Locate every blood parasite and identify its species.
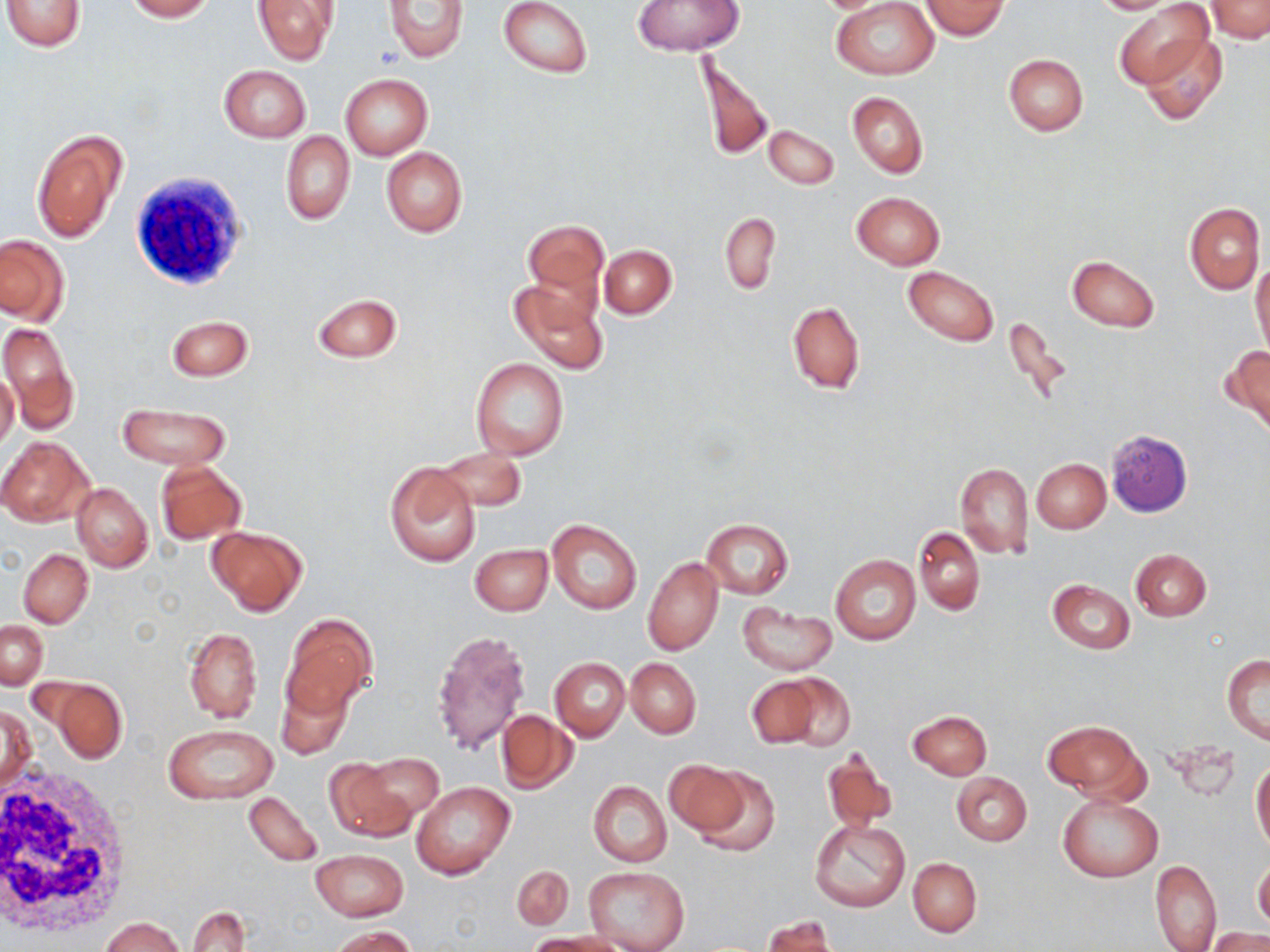

No blood parasites observed.

slide-level diagnosis = no evidence of blood parasites
stain = May-Grünwald-Giemsa
preparation = thin blood smear
white blood cell locations = approximate bounding boxes as named x1/y1/x2/y2 corners in pixels: (x1=129, y1=170, x2=247, y2=290), (x1=0, y1=766, x2=137, y2=936)
image size = 1270×952 pixels
field of view = single
magnification = 1000x
modality = optical microscopy
uninfected red blood cell locations = approximate bounding boxes as named x1/y1/x2/y2 corners in pixels: (x1=2, y1=0, x2=87, y2=52), (x1=123, y1=0, x2=213, y2=21), (x1=498, y1=0, x2=592, y2=78), (x1=1090, y1=0, x2=1180, y2=14), (x1=1205, y1=0, x2=1270, y2=42), (x1=251, y1=1, x2=337, y2=65), (x1=385, y1=1, x2=469, y2=61), (x1=633, y1=1, x2=744, y2=54), (x1=830, y1=1, x2=939, y2=80), (x1=921, y1=1, x2=1008, y2=39), (x1=1112, y1=1, x2=1213, y2=90), (x1=1138, y1=30, x2=1229, y2=125), (x1=695, y1=48, x2=774, y2=166), (x1=1003, y1=54, x2=1088, y2=136), (x1=218, y1=64, x2=311, y2=141), (x1=339, y1=73, x2=432, y2=160), (x1=846, y1=91, x2=927, y2=179), (x1=763, y1=125, x2=839, y2=189), (x1=31, y1=128, x2=127, y2=242), (x1=280, y1=132, x2=354, y2=225), (x1=381, y1=147, x2=468, y2=236), (x1=852, y1=192, x2=944, y2=268), (x1=1184, y1=202, x2=1265, y2=295), (x1=720, y1=213, x2=780, y2=294), (x1=521, y1=218, x2=609, y2=303), (x1=0, y1=235, x2=68, y2=324), (x1=599, y1=245, x2=676, y2=317), (x1=1067, y1=256, x2=1160, y2=331), (x1=1251, y1=261, x2=1270, y2=356), (x1=902, y1=267, x2=998, y2=346), (x1=509, y1=279, x2=607, y2=376), (x1=312, y1=294, x2=402, y2=363), (x1=786, y1=302, x2=865, y2=395), (x1=167, y1=315, x2=253, y2=380), (x1=0, y1=321, x2=80, y2=435), (x1=1224, y1=345, x2=1270, y2=433), (x1=470, y1=357, x2=568, y2=460), (x1=2, y1=359, x2=33, y2=446), (x1=0, y1=370, x2=19, y2=453), (x1=118, y1=404, x2=231, y2=470), (x1=0, y1=436, x2=92, y2=525), (x1=435, y1=447, x2=528, y2=512), (x1=1031, y1=459, x2=1110, y2=533), (x1=384, y1=461, x2=480, y2=567), (x1=954, y1=461, x2=1033, y2=559), (x1=155, y1=462, x2=245, y2=544), (x1=71, y1=483, x2=152, y2=571), (x1=547, y1=519, x2=642, y2=614), (x1=702, y1=520, x2=793, y2=599), (x1=206, y1=526, x2=308, y2=615), (x1=912, y1=527, x2=985, y2=615), (x1=470, y1=544, x2=552, y2=615), (x1=1131, y1=547, x2=1210, y2=621), (x1=19, y1=549, x2=93, y2=627), (x1=831, y1=555, x2=921, y2=645), (x1=644, y1=557, x2=724, y2=655), (x1=1047, y1=579, x2=1135, y2=654), (x1=738, y1=605, x2=837, y2=675), (x1=283, y1=615, x2=375, y2=715), (x1=1, y1=620, x2=48, y2=689), (x1=184, y1=626, x2=262, y2=723), (x1=431, y1=627, x2=534, y2=757), (x1=1222, y1=654, x2=1270, y2=744), (x1=625, y1=657, x2=701, y2=738), (x1=550, y1=658, x2=629, y2=739), (x1=745, y1=675, x2=822, y2=748), (x1=781, y1=675, x2=854, y2=750), (x1=278, y1=676, x2=355, y2=760), (x1=46, y1=678, x2=128, y2=763), (x1=1, y1=705, x2=34, y2=793), (x1=497, y1=709, x2=577, y2=794), (x1=908, y1=709, x2=992, y2=780), (x1=1044, y1=721, x2=1146, y2=801), (x1=161, y1=724, x2=278, y2=803), (x1=823, y1=748, x2=897, y2=834), (x1=359, y1=753, x2=443, y2=821), (x1=323, y1=758, x2=414, y2=841), (x1=665, y1=759, x2=747, y2=839), (x1=1251, y1=759, x2=1270, y2=853), (x1=687, y1=765, x2=781, y2=858), (x1=951, y1=771, x2=1032, y2=846), (x1=589, y1=781, x2=672, y2=867), (x1=412, y1=782, x2=515, y2=879), (x1=244, y1=790, x2=324, y2=868), (x1=1057, y1=792, x2=1163, y2=882), (x1=810, y1=819, x2=911, y2=913), (x1=310, y1=849, x2=407, y2=920), (x1=908, y1=857, x2=982, y2=937), (x1=1253, y1=858, x2=1270, y2=933), (x1=1150, y1=860, x2=1221, y2=952), (x1=511, y1=865, x2=574, y2=932), (x1=583, y1=866, x2=689, y2=952), (x1=188, y1=905, x2=249, y2=952), (x1=100, y1=916, x2=184, y2=952), (x1=762, y1=917, x2=838, y2=952), (x1=328, y1=925, x2=417, y2=951), (x1=1206, y1=929, x2=1270, y2=952), (x1=527, y1=933, x2=618, y2=952)